Report the malaria status of this cell.
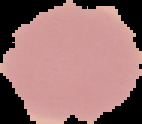

Uninfected.

preparation = thin blood smear
image type = cell region segmented out of the field of view; surrounding area masked to black
image size = 142×124 pixels